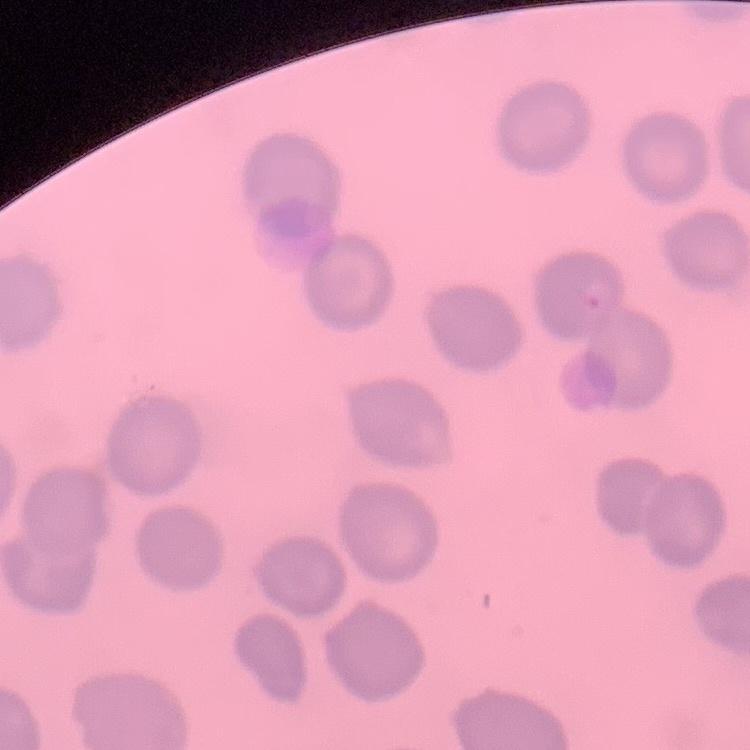
The erythrocytes show no rouleaux formation. Square crop of a larger photomicrograph. Thin peripheral smear. Stained with either Field's or Giemsa.